Point out each Plasmodium parasite.
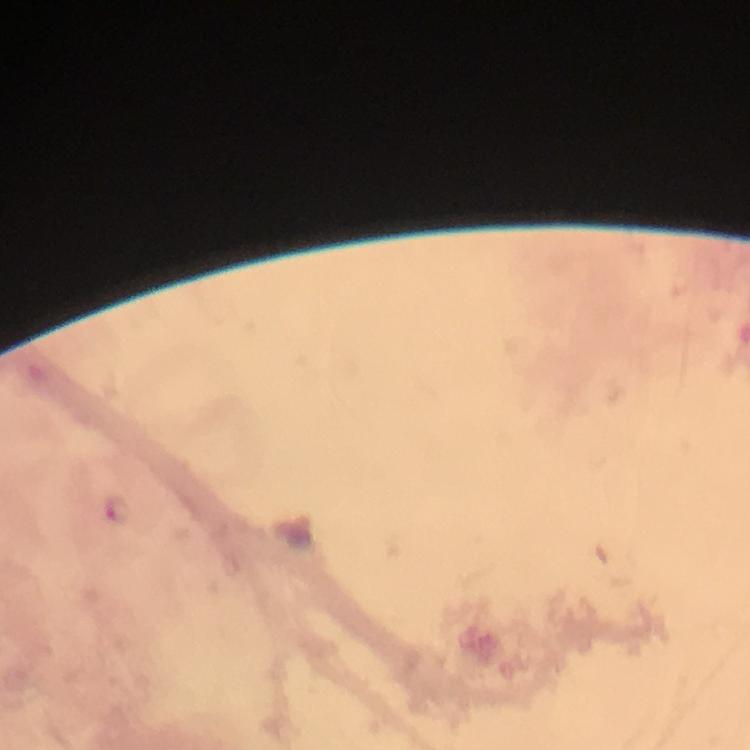

Approximate centers as (x, y) in pixels.
Plasmodium parasites: (116, 508).

Thick blood film. Cropped region of a single field of view. Smartphone photograph taken through a microscope. Giemsa stain. From a diagnostic examination for malaria. Immersion oil was used. At 100x magnification. Image is 750×750 pixels.